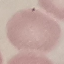
Malaria status: uninfected. Thin blood film. Acquired by smartphone through the microscope eyepiece. Automatically extracted cell patch, resized to 64 × 64 pixels. Giemsa stain.